State the preparation type.
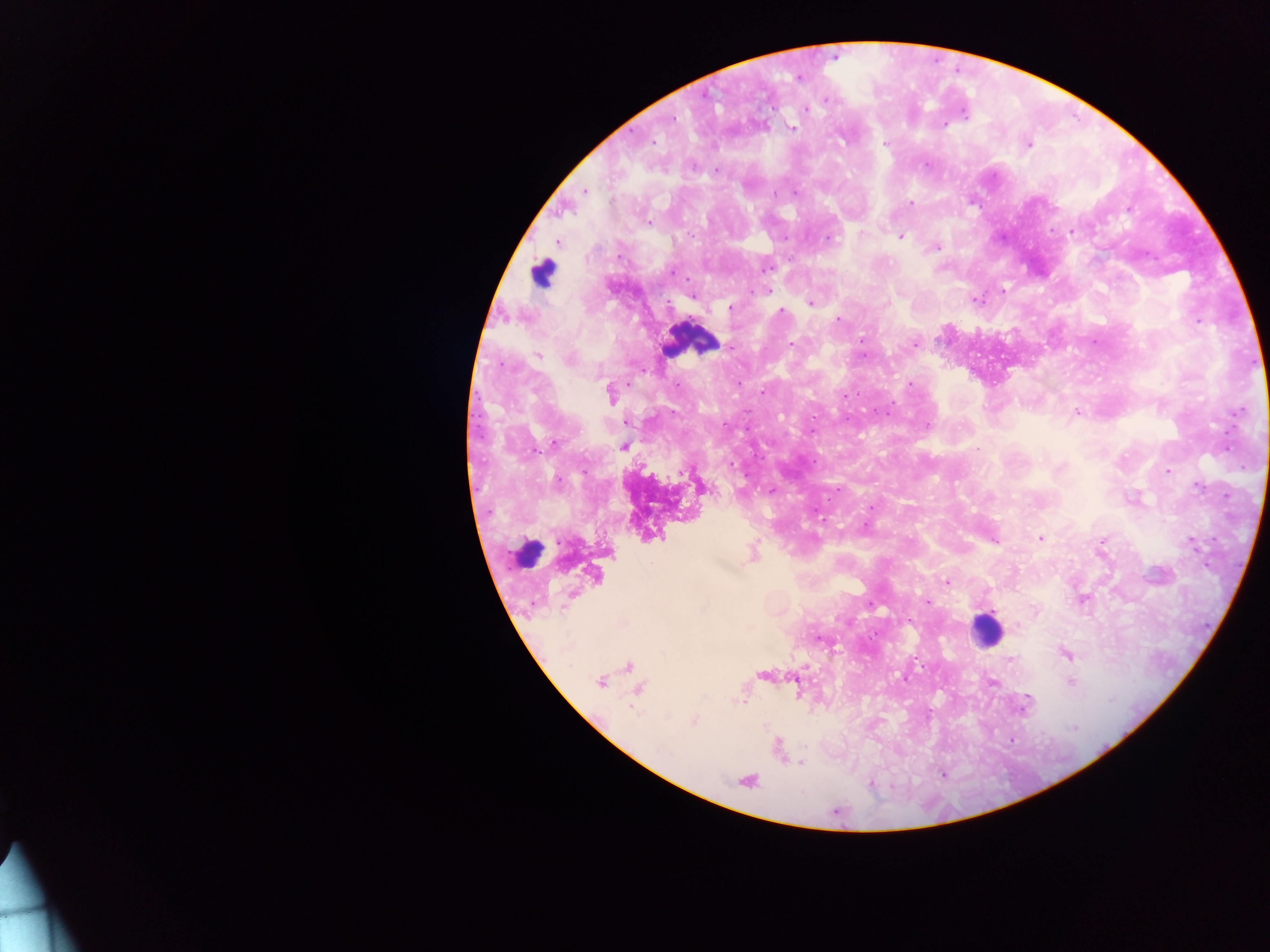

This is a thick smear.

Approximate centers as {x, y} in pixels. Leukocyte locations: {541, 270}, {693, 340}, {527, 550}, {986, 630}. Malaria parasite locations: {799, 77}, {826, 100}, {806, 108}, {965, 114}, {672, 119}, {946, 125}, {793, 127}, {653, 142}, {884, 144}, {1028, 144}, {926, 164}, {716, 170}, {585, 191}, {775, 192}, {796, 192}, {910, 204}, {1128, 209}, {649, 222}, {1071, 231}, {861, 234}, {901, 237}, {785, 238}, {829, 238}, {557, 242}, {938, 248}, {766, 269}, {753, 290}, {767, 290}, {1003, 291}, {692, 297}, {977, 300}, {810, 303}, {886, 303}, {730, 308}, {780, 311}, {838, 319}, {1198, 322}, {861, 340}, {792, 343}, {914, 344}, {863, 355}, {538, 356}, {570, 360}, {910, 383}, {739, 384}, {762, 392}, {611, 393}, {844, 396}, {1238, 411}, {1077, 412}, {927, 425}, {811, 432}, {554, 444}, {623, 446}, {978, 449}, {731, 466}, {1059, 468}, {1167, 471}, {558, 481}, {1199, 486}, {838, 489}, {871, 507}, {865, 526}, {1040, 538}, {1102, 540}, {995, 541}, {1192, 543}, {946, 581}, {927, 602}, {870, 605}, {1017, 625}, {818, 638}, {1065, 654}, {1010, 660}, {600, 682}, {1070, 682}, {993, 683}, {1111, 700}, {744, 703}, {1026, 703}, {695, 720}, {1074, 728}, {662, 750}, {800, 763}, {942, 775}, {871, 784}. Single field of view. Image is 1270×952 pixels. Photographed through a microscope with a mobile-phone camera. Collected in Ghana.